Assess the morphology of the erythrocytes.
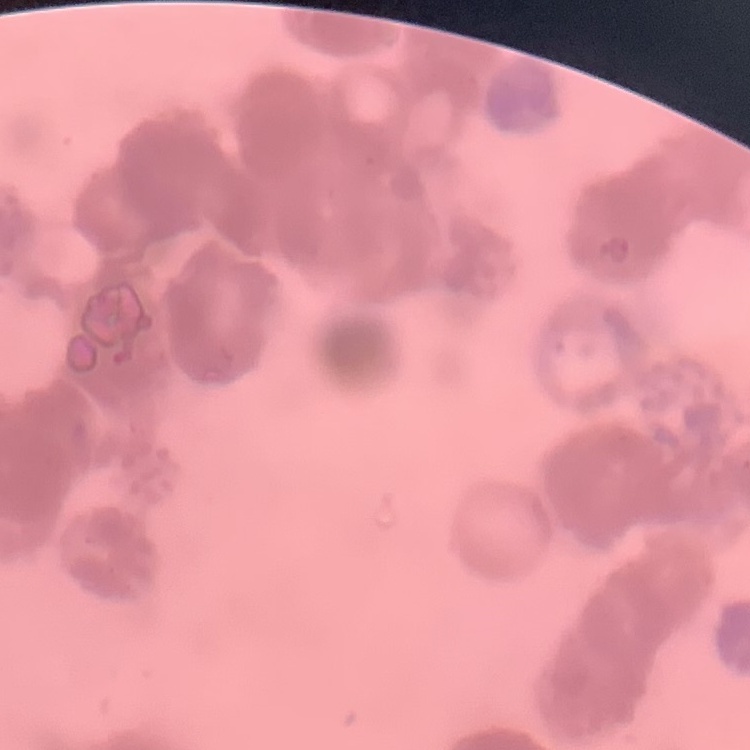

Rouleaux formation.

preparation = thin blood film
stain = Field's or Giemsa
image type = one tile cut from a larger photomicrograph